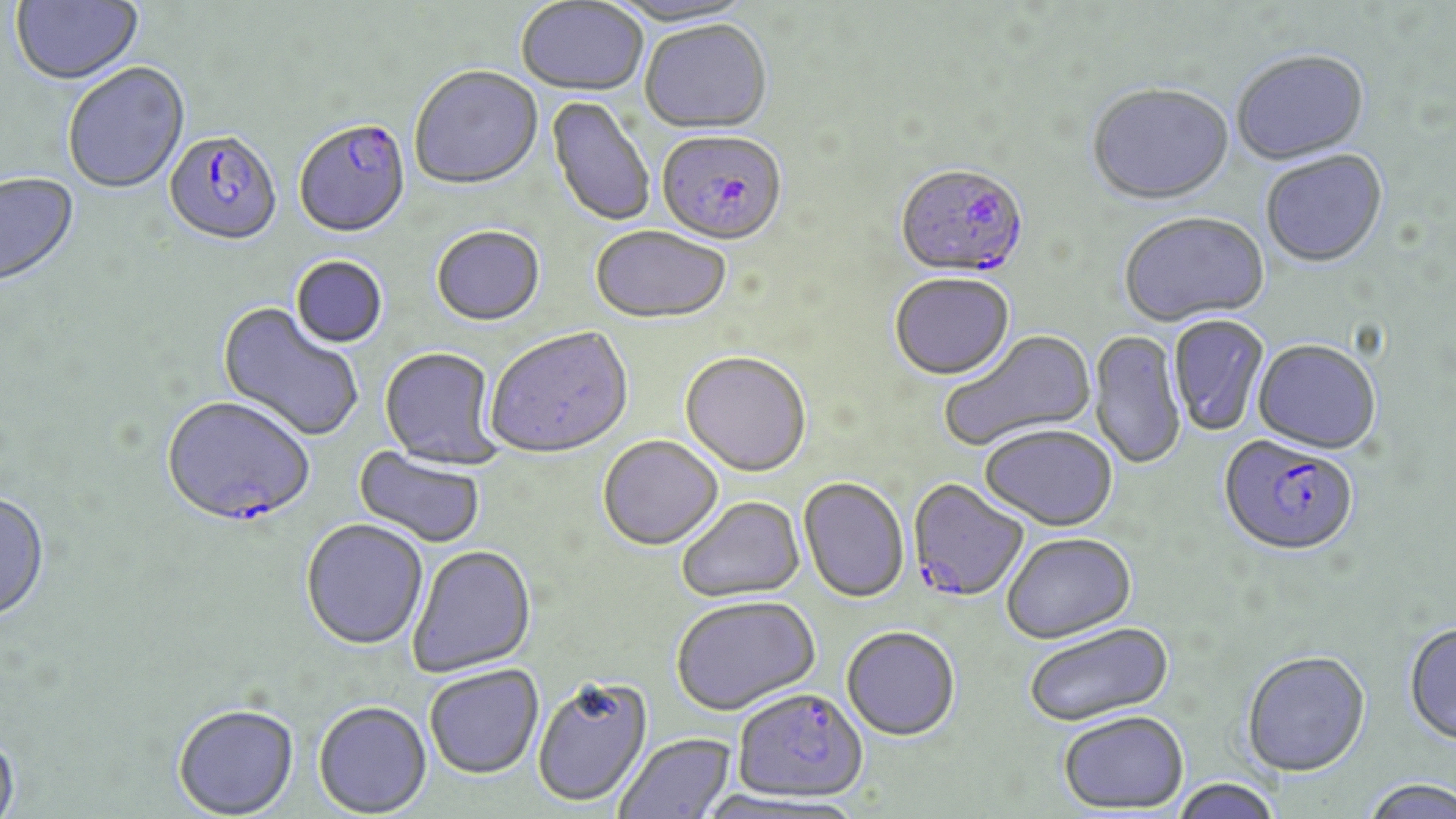
slide-level diagnosis = Plasmodium falciparum
stain = May-Grünwald-Giemsa
magnification = 1000x
uninfected red blood cell locations = approximate bounding boxes as (x1,y1)-(x2,y2) corner pairs in pixels: (10,0)-(144,87), (515,1)-(648,98), (611,1)-(760,30), (639,23)-(772,136), (1232,53)-(1370,167), (62,64)-(191,196), (408,68)-(544,193), (1087,86)-(1235,209), (546,96)-(656,228), (1261,152)-(1388,270), (0,173)-(81,291), (1120,214)-(1270,329), (590,227)-(731,327), (432,228)-(545,328), (290,256)-(388,350), (890,275)-(1015,383), (215,303)-(365,443), (1168,315)-(1269,437), (486,328)-(634,461), (940,330)-(1097,453), (1088,331)-(1187,471), (1253,342)-(1380,456), (379,348)-(502,468), (680,354)-(811,479), (980,427)-(1118,534), (597,437)-(724,553), (353,446)-(486,549), (798,479)-(909,605), (0,493)-(51,624), (677,498)-(805,604), (301,519)-(429,652), (1002,535)-(1136,646), (408,545)-(537,678), (671,597)-(821,718), (1024,623)-(1174,730), (1404,625)-(1456,748), (841,629)-(960,743), (1242,654)-(1372,779), (424,665)-(544,780), (532,677)-(654,808), (313,700)-(432,817), (173,703)-(299,818), (1059,714)-(1189,816), (0,728)-(21,818), (614,733)-(737,819), (1171,779)-(1282,819), (1360,779)-(1456,819)
image size = 1456×819 pixels
preparation = thin blood smear
modality = light microscopy
field of view = one of a larger specimen
Plasmodium falciparum-infected red blood cell locations = approximate bounding boxes as (x1,y1)-(x2,y2) corner pairs in pixels: (294,121)-(411,240), (163,131)-(283,249), (656,133)-(787,250), (894,166)-(1029,283), (162,397)-(317,528), (1218,439)-(1359,560), (907,480)-(1030,604), (732,691)-(867,807)